Name the blood parasite species.
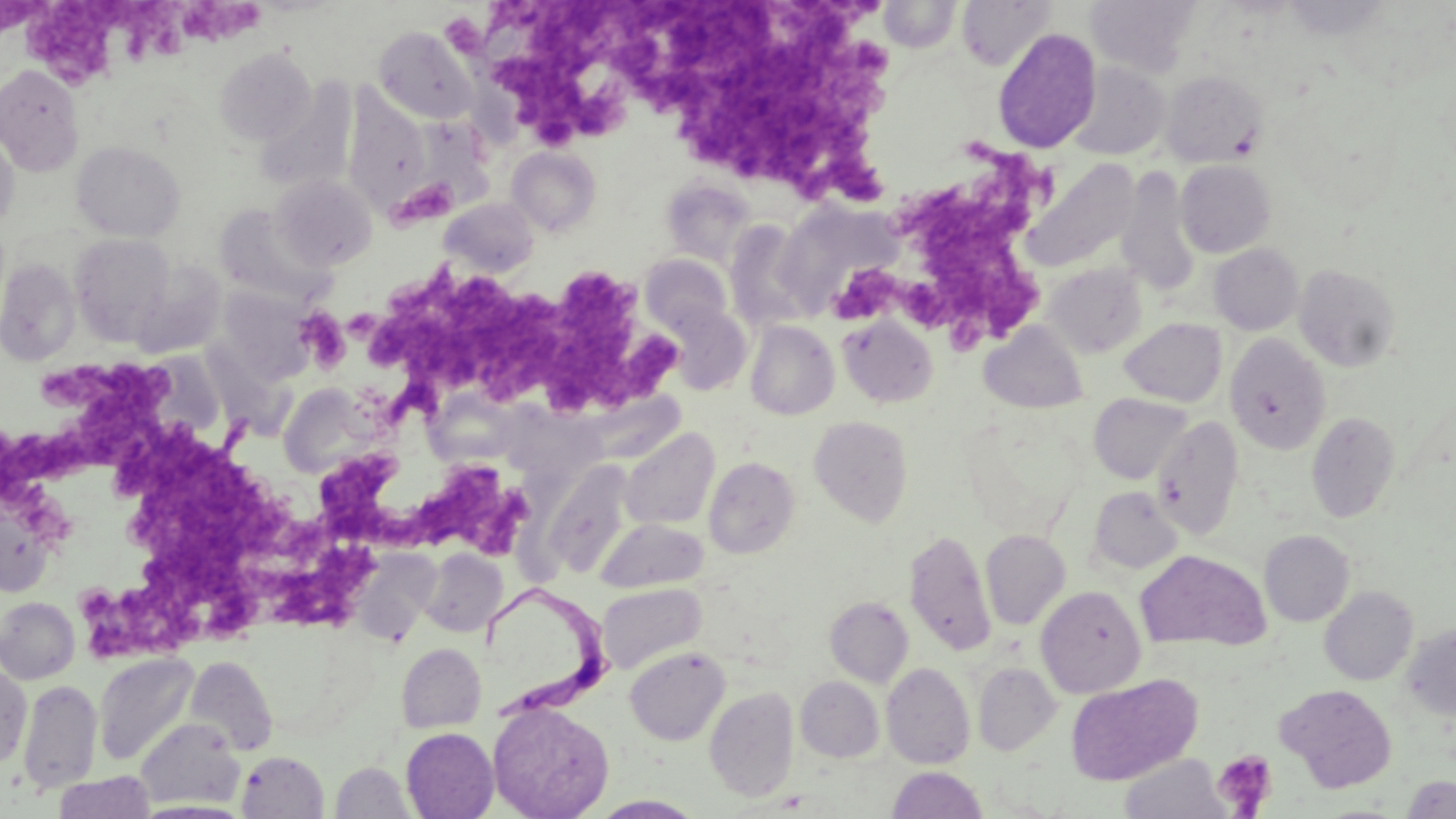
Trypanosoma brucei.

stain: May-Grünwald-Giemsa
platelet_locations: 'approximate bounding boxes as named x1/y1/x2/y2 corners in pixels: (x1=5, y1=0, x2=130, y2=89), (x1=113, y1=0, x2=188, y2=64), (x1=185, y1=3, x2=268, y2=45), (x1=491, y1=3, x2=713, y2=120), (x1=664, y1=3, x2=892, y2=202), (x1=496, y1=42, x2=615, y2=148), (x1=956, y1=139, x2=1056, y2=219), (x1=393, y1=178, x2=458, y2=225), (x1=905, y1=194, x2=1038, y2=348), (x1=377, y1=267, x2=681, y2=412), (x1=839, y1=269, x2=905, y2=321), (x1=300, y1=307, x2=351, y2=367), (x1=48, y1=361, x2=166, y2=466), (x1=117, y1=423, x2=306, y2=635), (x1=3, y1=431, x2=91, y2=503), (x1=314, y1=451, x2=424, y2=549), (x1=417, y1=463, x2=530, y2=556), (x1=263, y1=526, x2=374, y2=629), (x1=1211, y1=750, x2=1277, y2=816)'
image_size: 1456×819 pixels
uninfected_red_blood_cell_locations: 'approximate bounding boxes as named x1/y1/x2/y2 corners in pixels: (x1=957, y1=0, x2=1055, y2=71), (x1=1085, y1=0, x2=1200, y2=78), (x1=879, y1=1, x2=961, y2=51), (x1=373, y1=26, x2=478, y2=124), (x1=992, y1=27, x2=1102, y2=154), (x1=215, y1=48, x2=315, y2=146), (x1=1067, y1=62, x2=1170, y2=160), (x1=0, y1=64, x2=83, y2=177), (x1=1160, y1=69, x2=1268, y2=167), (x1=255, y1=81, x2=357, y2=195), (x1=344, y1=88, x2=430, y2=204), (x1=0, y1=130, x2=19, y2=232), (x1=71, y1=140, x2=185, y2=241), (x1=507, y1=147, x2=601, y2=236), (x1=1021, y1=158, x2=1140, y2=273), (x1=1176, y1=160, x2=1275, y2=257), (x1=1116, y1=169, x2=1201, y2=298), (x1=271, y1=175, x2=377, y2=271), (x1=662, y1=180, x2=755, y2=266), (x1=440, y1=199, x2=539, y2=278), (x1=775, y1=201, x2=902, y2=317), (x1=214, y1=204, x2=330, y2=305), (x1=725, y1=221, x2=814, y2=331), (x1=70, y1=234, x2=174, y2=345), (x1=1209, y1=243, x2=1303, y2=335), (x1=640, y1=254, x2=732, y2=334), (x1=0, y1=257, x2=81, y2=365), (x1=131, y1=263, x2=226, y2=360), (x1=1043, y1=263, x2=1147, y2=358), (x1=1293, y1=263, x2=1401, y2=372), (x1=215, y1=287, x2=318, y2=383), (x1=661, y1=302, x2=750, y2=394), (x1=838, y1=315, x2=938, y2=407), (x1=1120, y1=318, x2=1227, y2=407), (x1=745, y1=320, x2=839, y2=420), (x1=980, y1=321, x2=1087, y2=413), (x1=1225, y1=334, x2=1331, y2=455), (x1=278, y1=384, x2=379, y2=478), (x1=1089, y1=393, x2=1193, y2=484), (x1=1307, y1=411, x2=1401, y2=523), (x1=809, y1=416, x2=913, y2=527), (x1=1152, y1=416, x2=1244, y2=539), (x1=619, y1=429, x2=719, y2=530), (x1=704, y1=456, x2=800, y2=558), (x1=543, y1=462, x2=634, y2=578), (x1=1088, y1=485, x2=1183, y2=575), (x1=597, y1=517, x2=709, y2=592), (x1=904, y1=528, x2=996, y2=656), (x1=980, y1=530, x2=1070, y2=630), (x1=1259, y1=530, x2=1354, y2=626), (x1=420, y1=549, x2=507, y2=637), (x1=1135, y1=550, x2=1271, y2=652), (x1=598, y1=583, x2=706, y2=675), (x1=1036, y1=585, x2=1147, y2=698), (x1=1320, y1=585, x2=1418, y2=686), (x1=0, y1=596, x2=80, y2=684), (x1=825, y1=596, x2=914, y2=687), (x1=1402, y1=624, x2=1456, y2=721), (x1=397, y1=643, x2=486, y2=732), (x1=624, y1=646, x2=730, y2=745), (x1=93, y1=653, x2=200, y2=766), (x1=185, y1=656, x2=278, y2=756), (x1=973, y1=662, x2=1061, y2=756), (x1=0, y1=663, x2=31, y2=770), (x1=881, y1=663, x2=975, y2=769), (x1=1066, y1=675, x2=1200, y2=785), (x1=796, y1=676, x2=885, y2=762), (x1=18, y1=679, x2=102, y2=793), (x1=1275, y1=684, x2=1398, y2=792), (x1=705, y1=686, x2=799, y2=801), (x1=487, y1=701, x2=614, y2=819), (x1=136, y1=718, x2=244, y2=809), (x1=400, y1=727, x2=498, y2=819), (x1=237, y1=751, x2=329, y2=818), (x1=1119, y1=754, x2=1230, y2=819), (x1=331, y1=761, x2=415, y2=818), (x1=887, y1=766, x2=988, y2=819), (x1=53, y1=772, x2=154, y2=818), (x1=1402, y1=775, x2=1456, y2=818), (x1=590, y1=794, x2=707, y2=818), (x1=133, y1=800, x2=251, y2=818)'
preparation: thin blood film
magnification: 1000x
modality: light microscopy
field_of_view: single
trypanosoma_brucei_locations: 'approximate bounding boxes as named x1/y1/x2/y2 corners in pixels: (x1=480, y1=585, x2=615, y2=725)'